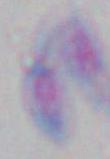

Summary:
  - Identification: Toxoplasma gondii
  - Magnification: 1000x
  - Modality: photomicrograph